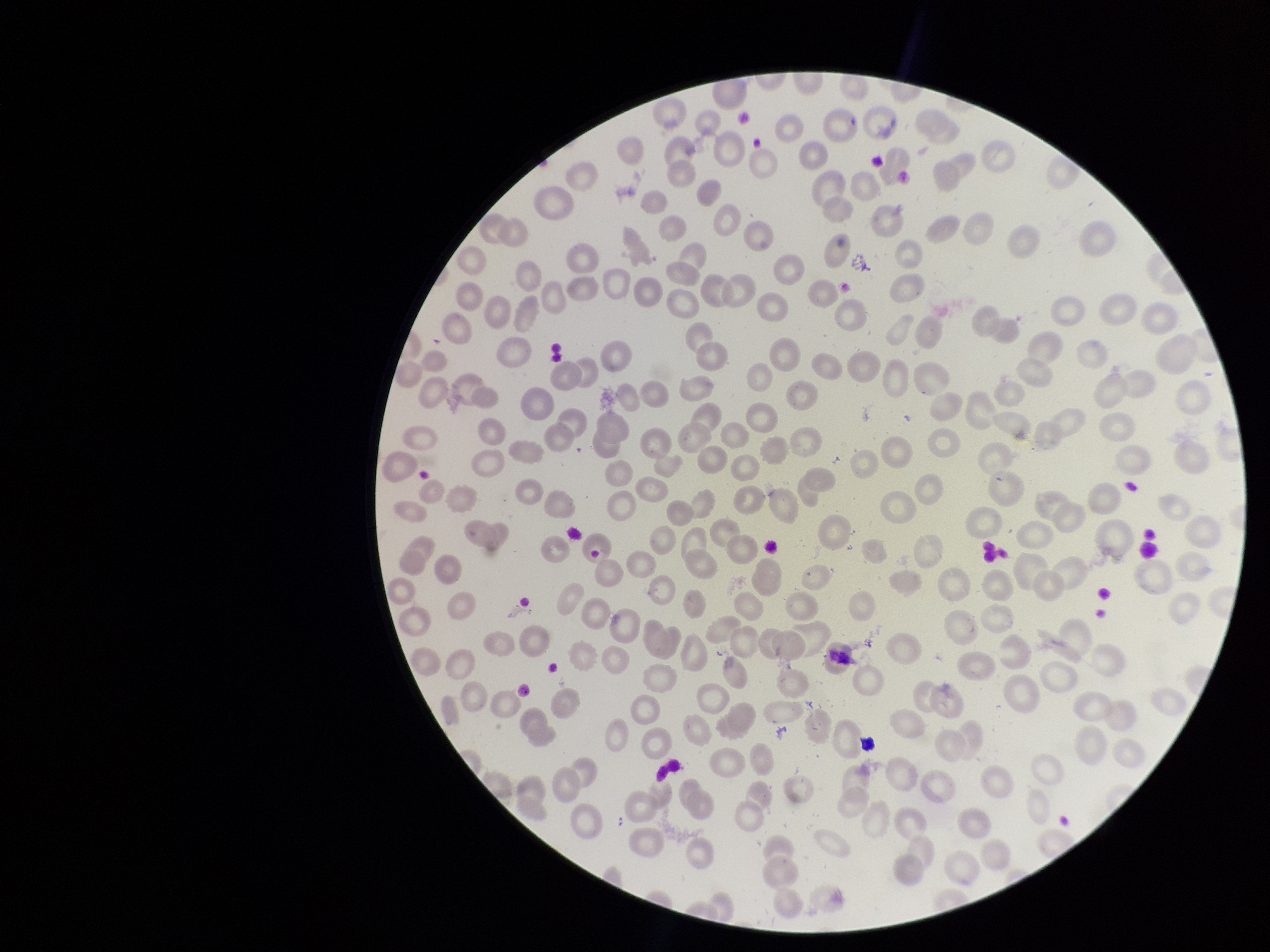

Parasitized red blood cell count: 0. Preparation: thin blood smear. Single field of view. Parasitized red blood cells: none seen. Smartphone photograph taken through the eyepiece of a microscope. Image is 1270×952 pixels. Giemsa stain. Patient malaria status: positive. Species reported for this patient: Plasmodium falciparum. Red blood cell count: 178.